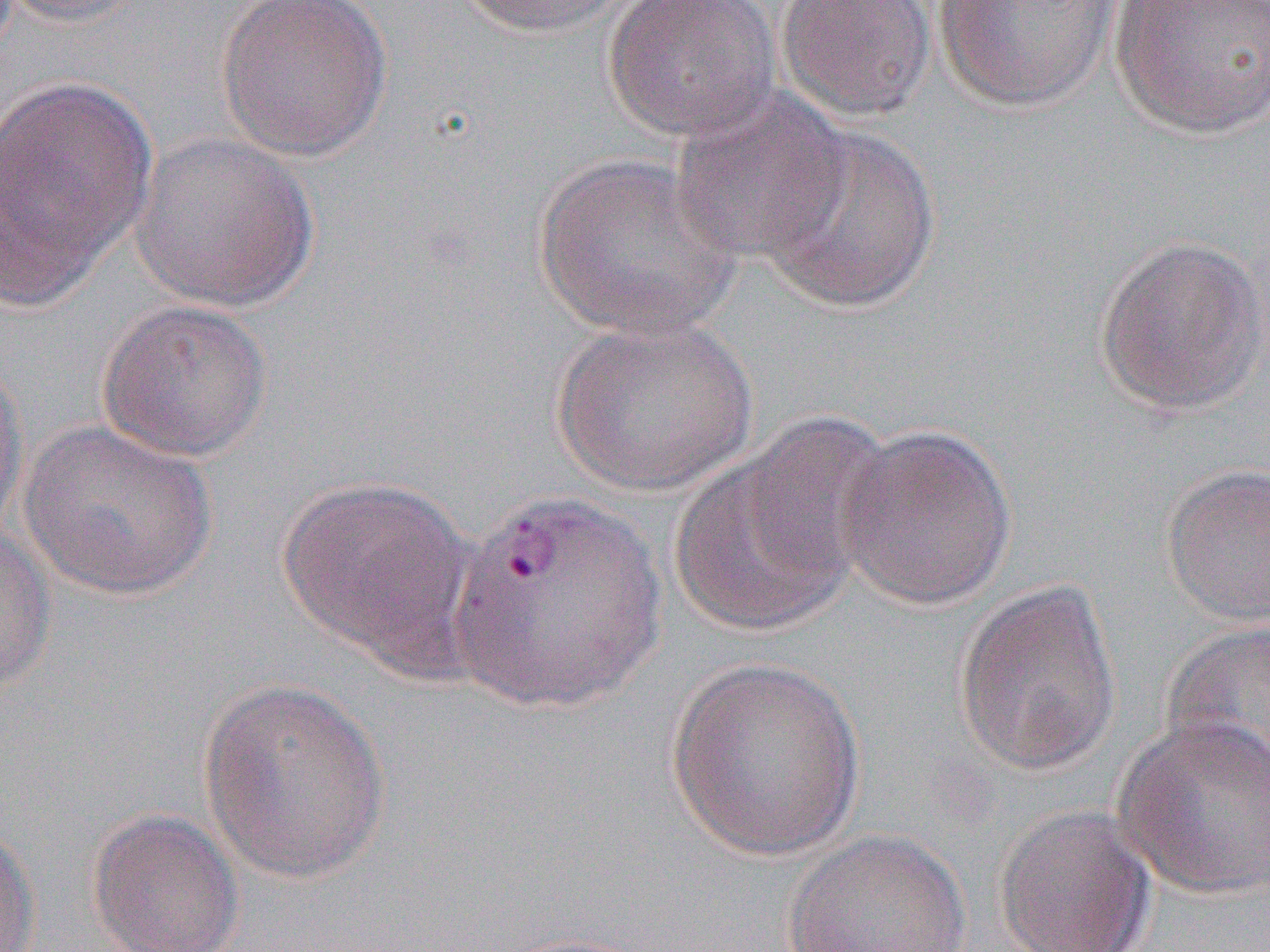

slide-level diagnosis = Plasmodium vivax
uninfected red blood cell locations = approximate bounding boxes as named x1/y1/x2/y2 corners in pixels: (x1=1, y1=0, x2=150, y2=29), (x1=215, y1=0, x2=394, y2=162), (x1=453, y1=0, x2=642, y2=38), (x1=601, y1=0, x2=781, y2=143), (x1=775, y1=0, x2=939, y2=124), (x1=1109, y1=0, x2=1270, y2=139), (x1=930, y1=1, x2=1124, y2=113), (x1=0, y1=74, x2=158, y2=308), (x1=668, y1=85, x2=853, y2=267), (x1=757, y1=121, x2=942, y2=316), (x1=127, y1=131, x2=319, y2=312), (x1=533, y1=152, x2=744, y2=343), (x1=1092, y1=233, x2=1269, y2=418), (x1=95, y1=296, x2=274, y2=465), (x1=548, y1=313, x2=760, y2=498), (x1=0, y1=345, x2=30, y2=548), (x1=18, y1=419, x2=218, y2=602), (x1=834, y1=422, x2=1018, y2=612), (x1=667, y1=443, x2=864, y2=639), (x1=1161, y1=462, x2=1270, y2=627), (x1=276, y1=476, x2=478, y2=673), (x1=1, y1=523, x2=56, y2=698), (x1=952, y1=580, x2=1124, y2=778), (x1=1161, y1=620, x2=1270, y2=792), (x1=664, y1=657, x2=869, y2=860), (x1=196, y1=677, x2=393, y2=884), (x1=1112, y1=714, x2=1270, y2=901), (x1=990, y1=805, x2=1157, y2=952), (x1=86, y1=808, x2=245, y2=952), (x1=0, y1=821, x2=39, y2=952), (x1=780, y1=828, x2=972, y2=952)
field of view = single
modality = optical microscopy
image size = 1270×952 pixels
magnification = 1000x
preparation = thin blood film